Give the extent of all Plasmodium falciparum-infected red blood cells.
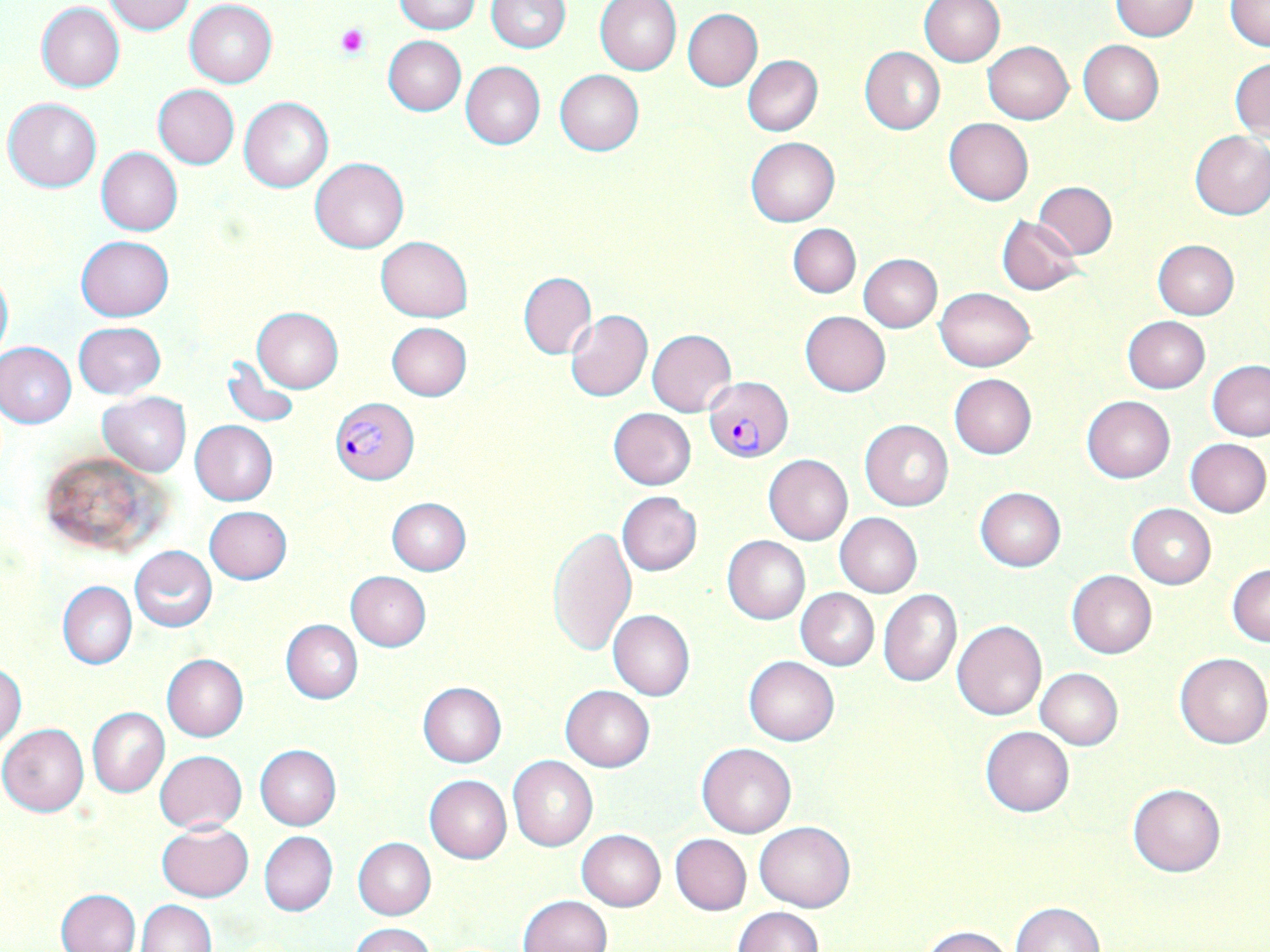
Approximate bounding boxes as [x1, y1, x2, y2] in pixels.
Plasmodium falciparum-infected red blood cells: [706, 377, 792, 461], [330, 396, 419, 484].

Platelet locations: [336, 26, 368, 58]. Uninfected red blood cell locations: [394, 0, 480, 33], [487, 0, 571, 51], [596, 0, 682, 75], [919, 0, 1004, 67], [1109, 0, 1201, 41], [1225, 0, 1270, 52], [102, 1, 196, 34], [184, 1, 277, 88], [37, 2, 125, 92], [683, 8, 763, 90], [383, 36, 466, 116], [1078, 41, 1163, 124], [982, 42, 1073, 123], [859, 46, 945, 135], [742, 55, 822, 136], [1230, 57, 1270, 141], [461, 62, 546, 150], [555, 70, 643, 155], [153, 84, 239, 168], [4, 97, 102, 192], [239, 97, 333, 192], [943, 118, 1033, 206], [1189, 131, 1270, 220], [746, 137, 840, 226], [97, 147, 182, 236], [88, 151, 177, 326], [310, 157, 409, 253], [1033, 182, 1116, 258], [996, 216, 1085, 296], [789, 223, 861, 297], [75, 236, 174, 321], [376, 236, 473, 322], [1151, 240, 1239, 320], [859, 254, 942, 332], [0, 264, 12, 366], [519, 273, 597, 358], [935, 287, 1034, 371], [251, 307, 343, 391], [565, 308, 653, 402], [801, 311, 890, 396], [1123, 315, 1210, 393], [74, 322, 166, 399], [386, 322, 473, 400], [647, 329, 736, 416], [0, 341, 77, 428], [222, 355, 300, 428], [1207, 361, 1270, 440], [949, 373, 1037, 459], [97, 392, 191, 476], [1082, 396, 1176, 483], [608, 407, 696, 489], [860, 419, 954, 511], [190, 421, 278, 505], [1185, 438, 1270, 516], [36, 451, 166, 555], [763, 455, 852, 545], [975, 487, 1066, 571], [617, 492, 702, 576], [387, 498, 472, 575], [1126, 504, 1216, 589], [204, 505, 292, 583], [833, 512, 922, 598], [548, 526, 637, 655], [722, 535, 810, 624], [130, 546, 218, 631], [1227, 563, 1270, 646], [345, 570, 431, 651], [1067, 571, 1156, 658], [57, 581, 137, 669], [878, 588, 962, 688], [795, 589, 878, 670], [609, 609, 695, 701], [951, 619, 1048, 720], [281, 620, 363, 703], [1175, 652, 1270, 749], [162, 654, 248, 741], [743, 656, 839, 746], [0, 664, 25, 748], [1036, 669, 1123, 749], [418, 682, 507, 767], [560, 686, 654, 771], [88, 707, 170, 797], [0, 723, 89, 816], [981, 726, 1074, 817], [696, 742, 797, 837], [255, 745, 340, 830], [154, 750, 247, 833], [508, 756, 598, 851], [424, 775, 512, 863], [1128, 782, 1226, 877], [756, 820, 855, 912], [155, 821, 254, 901], [577, 829, 666, 910], [258, 831, 337, 917], [670, 833, 751, 915], [353, 838, 435, 919], [56, 888, 140, 951], [519, 895, 612, 952], [137, 899, 216, 951], [1010, 902, 1104, 952], [732, 906, 822, 952], [351, 922, 435, 952], [919, 926, 1015, 952]. Slide-level diagnosis: Plasmodium falciparum. Light microscopy. Image is 1270×952 pixels. One field of a larger specimen. Captured at 1000x magnification. Thin blood film. May-Grünwald-Giemsa-stained preparation.